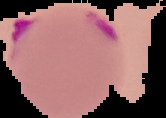
Summary:
  - Preparation: thin blood smear
  - Image size: 166×118 pixels
  - Result: Plasmodium parasites detected
  - Image type: cell region segmented out of the field of view; surrounding area masked to black